State which parasite is depicted.
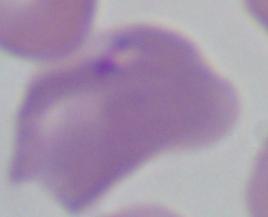

This is Babesia.

Micrograph. Captured at 1000x magnification.